State which parasite is depicted.
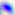

Toxoplasma gondii.

400x magnification. Micrograph.